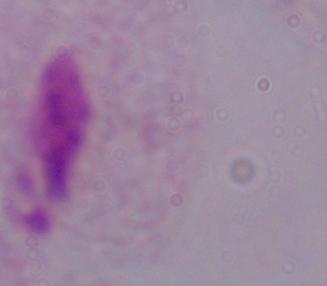
A trichomonad is seen. Photomicrograph. Captured at 1000x magnification.